State which parasite is depicted.
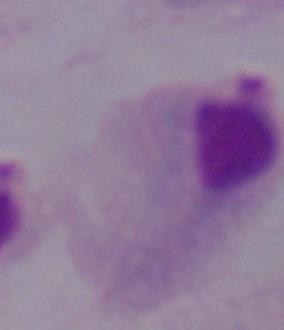

A trichomonad.

Summary:
  - Magnification: 1000x
  - Modality: micrograph